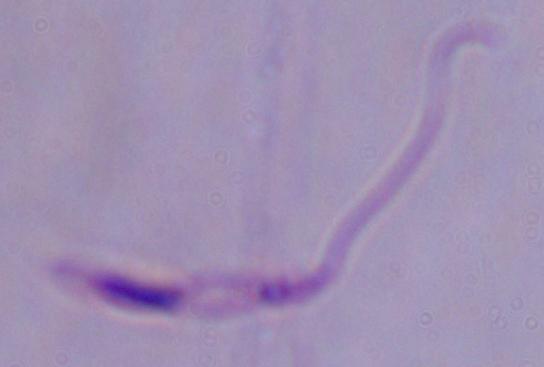
Summary:
  - Identification: Leishmania
  - Modality: photomicrograph
  - Magnification: 1000x